State which parasite is depicted.
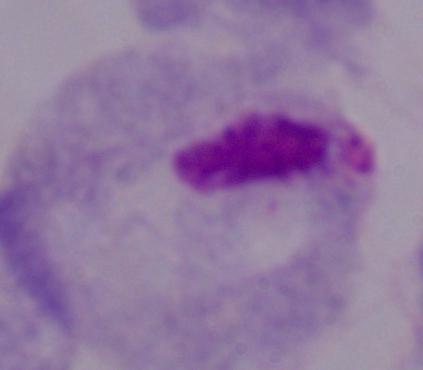

A trichomonad.

{
  "magnification": "1000x",
  "modality": "micrograph"
}